Report the malaria status of this cell.
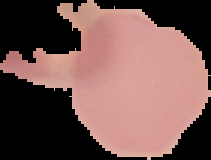
It is uninfected.

Image is 211×160 pixels. Segmented cell region on a black background. From a thin blood smear.